State which cell type is depicted.
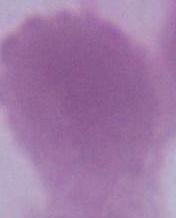
This is an erythrocyte.

Summary:
  - Magnification: 1000x
  - Modality: micrograph